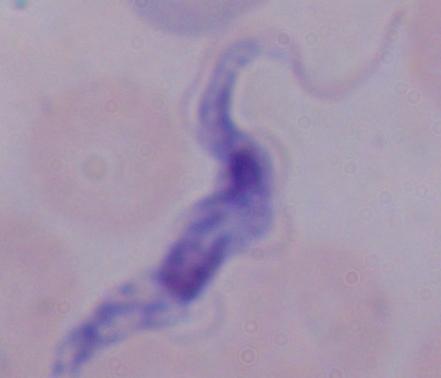

identification: trypanosome
magnification: 1000x
modality: micrograph